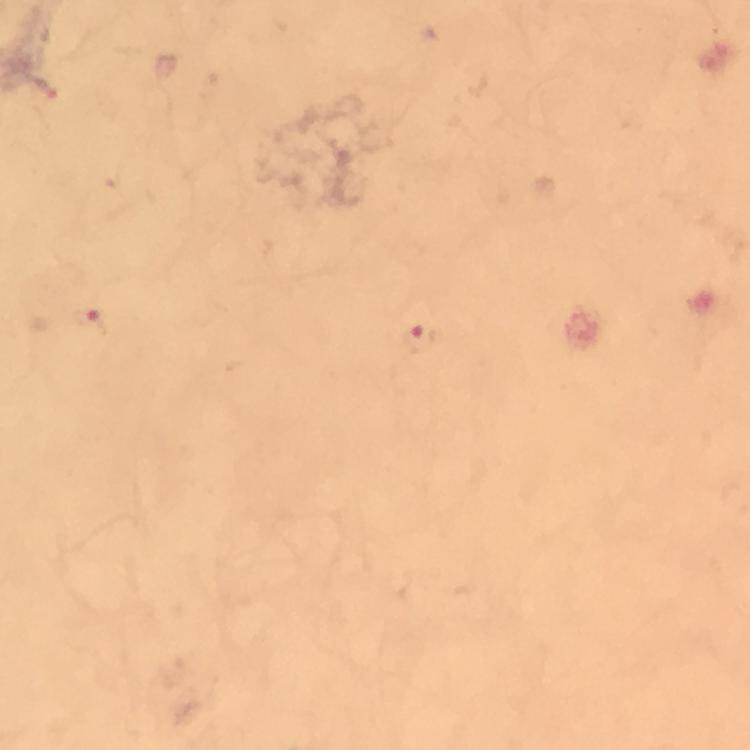
Approximate centers as [x, y] in pixels.
Summary:
  - Malaria parasite locations: [90, 321], [418, 340]
  - Immersion oil: used
  - Stain: Giemsa
  - Cropped from: a single field of view
  - Preparation: thick blood smear
  - Image size: 750×750 pixels
  - Capture: smartphone photograph through a microscope
  - Magnification: 100x
  - Context: from a malaria diagnostic workup